Report the malaria status of this cell.
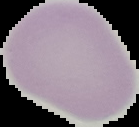

It is uninfected.

Summary:
  - Image size: 139×127 pixels
  - Preparation: thin blood film
  - Image type: segmented cell region with the area outside set to black